Report the malaria status of this cell.
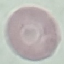

Uninfected.

Summary:
  - Preparation: thin blood smear
  - Stain: Giemsa
  - Image type: cell patch, automatically extracted from a larger field of view and resized to 64 × 64 pixels
  - Capture: smartphone through the microscope eyepiece